Give the position of every Plasmodium parasite visible.
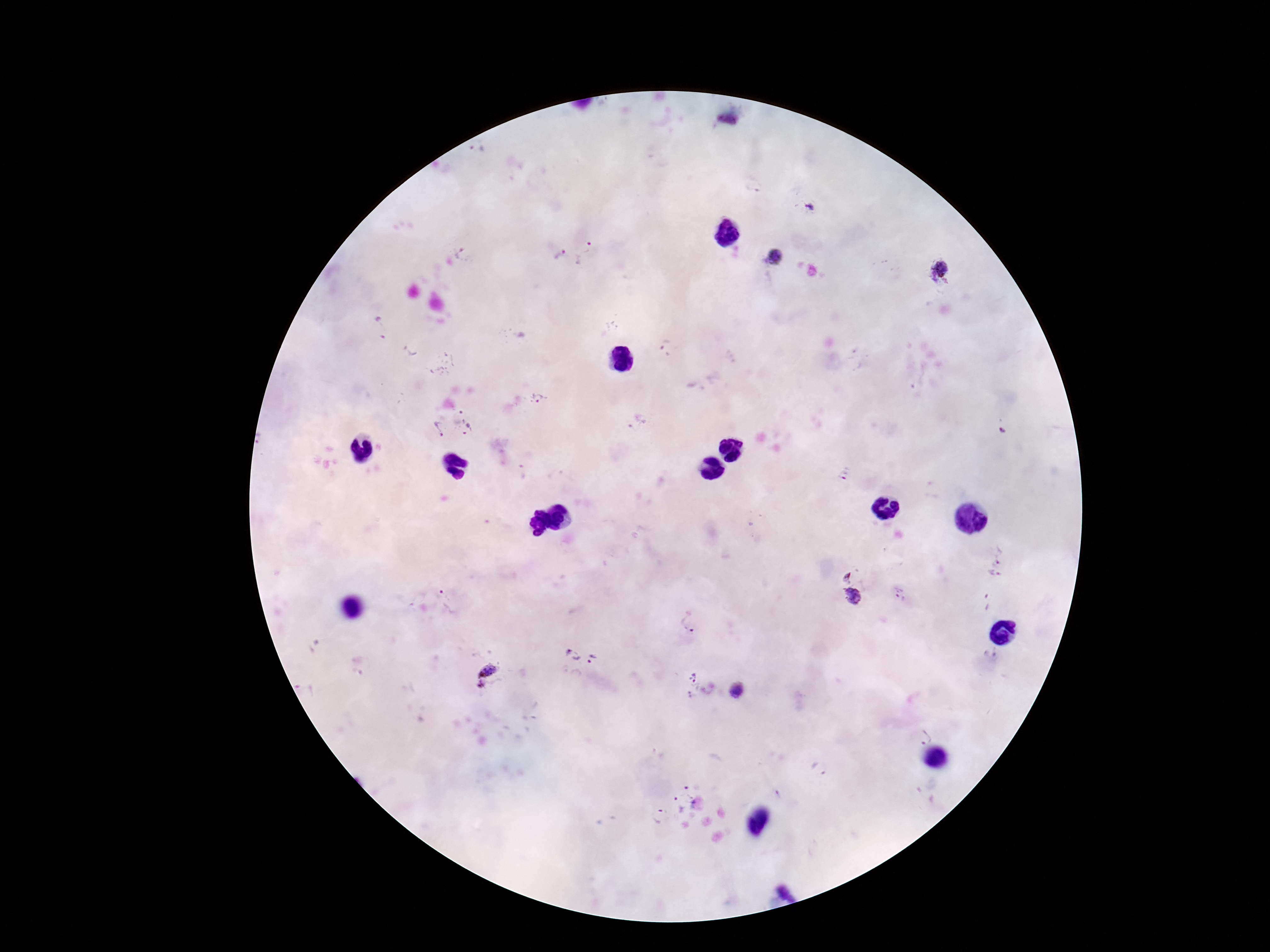

Approximate centers as {x, y} in pixels.
Plasmodium parasites: {727, 122}, {477, 151}, {811, 206}, {557, 253}, {584, 253}, {461, 254}, {774, 257}, {942, 268}, {380, 328}, {667, 350}, {539, 398}, {467, 421}, {437, 428}, {844, 474}, {999, 557}, {993, 575}, {845, 576}, {898, 595}, {852, 596}, {451, 602}, {986, 603}, {687, 622}, {573, 655}, {594, 660}, {488, 670}, {693, 677}, {480, 686}, {306, 689}, {737, 690}, {923, 737}, {818, 769}, {684, 794}, {658, 815}.

Summary:
  - Magnification: 100x
  - Image size: 1270×952 pixels
  - Capture: smartphone camera through the microscope eyepiece
  - Stain: Giemsa
  - Field of view: one from this slide
  - Preparation: thick blood smear
  - Patient malaria status: infected